State the blood parasite species.
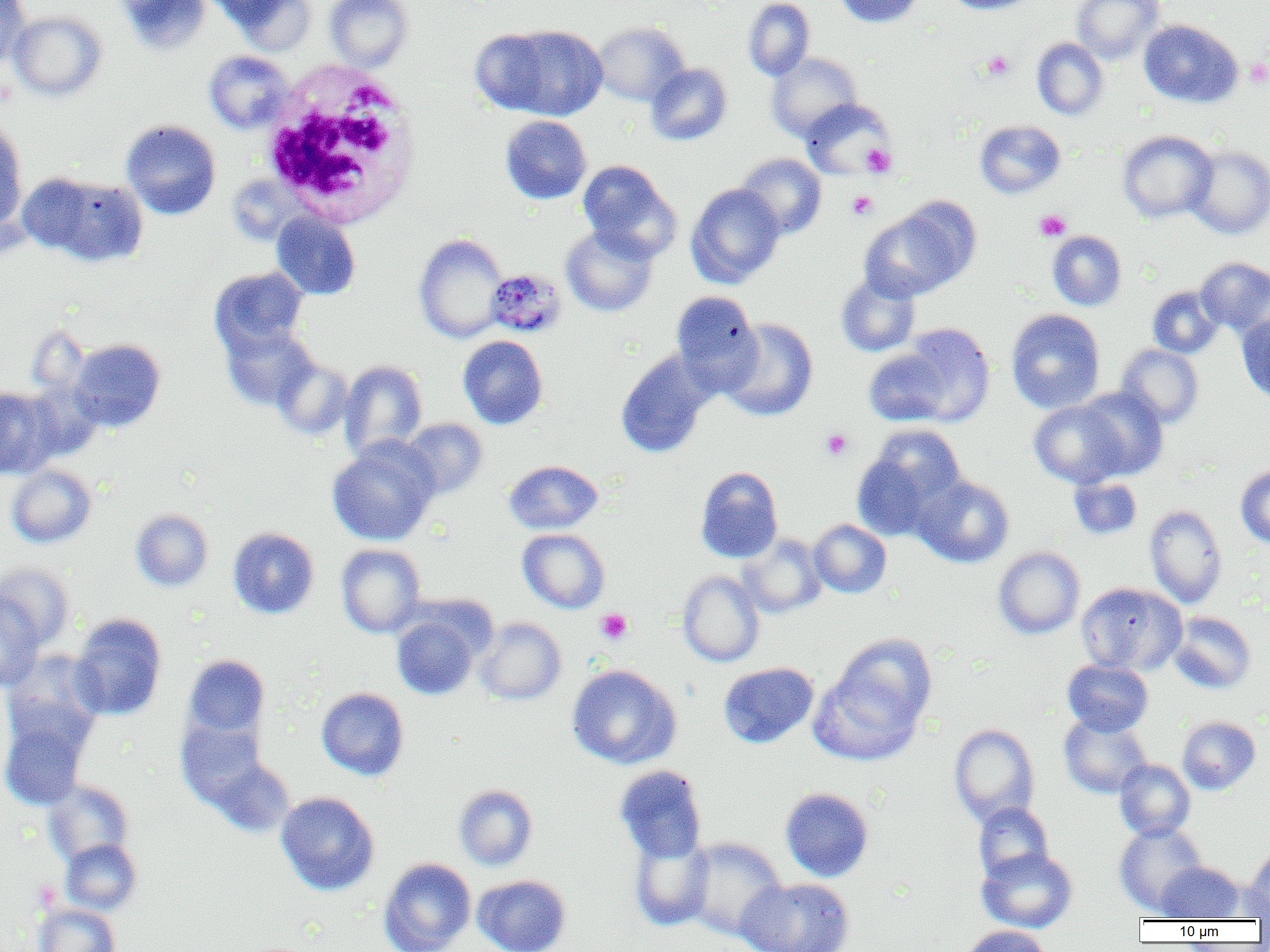

Plasmodium malariae.

Summary:
  - Coordinate format: approximate bounding boxes as (x1, y1, x2, y2) in pixels
  - Platelet locations: (982, 50, 1015, 81), (1245, 59, 1270, 87), (861, 144, 896, 177), (847, 190, 878, 220), (1034, 210, 1071, 241), (821, 429, 853, 460), (595, 608, 633, 645)
  - Plasmodium malariae-infected red blood cell locations: (486, 268, 565, 337)
  - Uninfected red blood cell locations: (0, 0, 32, 67), (116, 0, 211, 55), (226, 0, 317, 56), (324, 0, 413, 71), (743, 0, 815, 81), (835, 0, 923, 27), (943, 0, 1039, 15), (1071, 0, 1165, 63), (8, 10, 107, 102), (1138, 19, 1243, 108), (592, 22, 689, 106), (486, 24, 608, 121), (1032, 37, 1108, 120), (204, 50, 295, 133), (767, 52, 863, 142), (645, 63, 732, 146), (800, 99, 894, 179), (500, 115, 592, 204), (0, 119, 28, 229), (121, 119, 221, 220), (975, 120, 1065, 198), (1117, 130, 1217, 222), (1186, 145, 1270, 239), (736, 153, 827, 239), (578, 161, 680, 262), (30, 174, 148, 267), (686, 183, 785, 288), (859, 205, 973, 301), (271, 211, 361, 300), (561, 225, 658, 317), (1048, 230, 1127, 311), (413, 233, 508, 343), (1195, 257, 1270, 335), (209, 267, 308, 354), (835, 272, 920, 357), (1147, 286, 1224, 359), (671, 291, 763, 393), (1006, 309, 1105, 414), (1236, 313, 1270, 404), (720, 318, 818, 421), (221, 323, 319, 411), (900, 323, 995, 426), (458, 335, 548, 429), (68, 338, 165, 432), (1116, 344, 1203, 428), (863, 348, 952, 426), (615, 350, 715, 458), (272, 357, 354, 440), (339, 360, 427, 461), (1074, 386, 1169, 480), (0, 387, 58, 479), (1029, 400, 1127, 488), (400, 418, 488, 499), (853, 426, 966, 539), (327, 438, 439, 546), (504, 460, 603, 534), (6, 464, 97, 548), (1235, 465, 1270, 548), (695, 466, 783, 563), (913, 475, 1015, 568), (1068, 476, 1142, 540), (1144, 504, 1228, 608), (130, 508, 213, 592), (809, 519, 891, 598), (228, 527, 319, 619), (517, 529, 610, 613), (737, 533, 827, 618), (336, 544, 426, 638), (993, 546, 1085, 639), (0, 562, 75, 650), (677, 571, 765, 667), (1076, 582, 1186, 675), (0, 591, 44, 691), (1167, 611, 1256, 693), (69, 613, 167, 720), (392, 613, 481, 700), (475, 617, 566, 705), (810, 643, 933, 766), (2, 651, 106, 757), (182, 654, 270, 742), (1063, 659, 1153, 736), (718, 662, 819, 748), (566, 664, 682, 769), (316, 687, 409, 781), (0, 711, 92, 811), (1059, 714, 1152, 798), (1177, 716, 1260, 794), (176, 717, 270, 809), (949, 723, 1040, 826), (205, 755, 295, 838), (1114, 758, 1195, 841), (614, 765, 707, 864), (43, 780, 134, 866), (453, 784, 538, 871), (780, 787, 874, 882), (276, 791, 379, 895), (973, 802, 1054, 882), (1114, 822, 1207, 915), (628, 830, 715, 931), (683, 837, 787, 940), (60, 838, 142, 915), (1243, 846, 1270, 919), (977, 847, 1078, 933), (379, 857, 476, 952), (1157, 861, 1247, 922), (472, 874, 571, 952), (736, 877, 855, 951), (33, 904, 120, 952), (960, 925, 1053, 952)
  - White blood cell locations: (261, 62, 424, 228)
  - Field of view: single
  - Image size: 1270×952 pixels
  - Magnification: 1000x
  - Modality: light microscopy
  - Preparation: thin blood smear